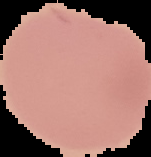 The area outside the segmented cell region is set to black. Malaria status: uninfected. From a thin blood smear. Image is 151×157 pixels.